Identify the cell.
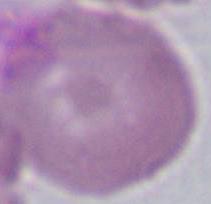

An erythrocyte.

1000x magnification. Micrograph.